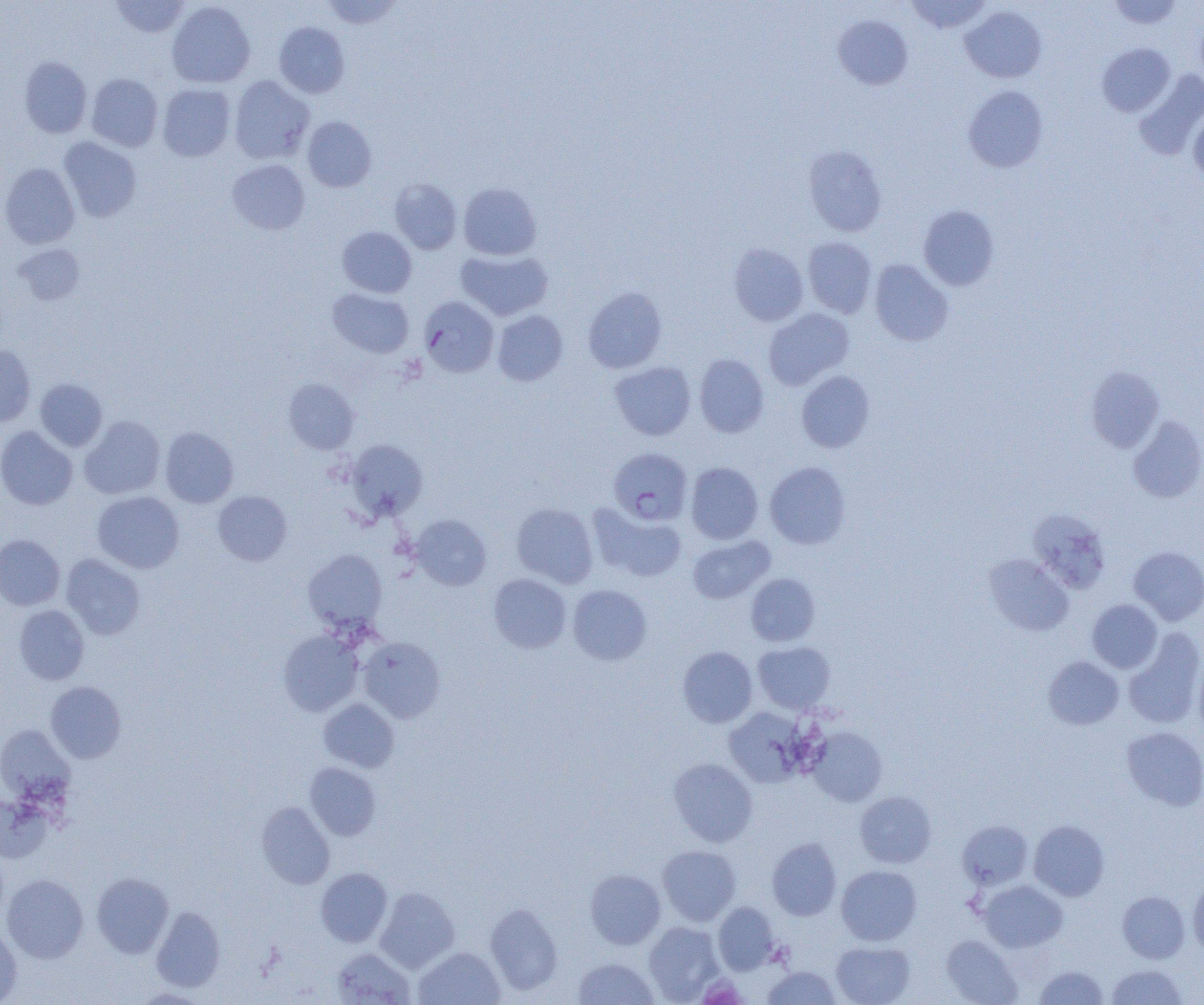

slide-level diagnosis = Plasmodium falciparum
image size = 1204×1005 pixels
modality = light microscopy
magnification = 1000x
field of view = one of a larger specimen
Plasmodium falciparum-infected red blood cell locations = approximate bounding boxes as [x1, y1, x2, y2] in pixels: [419, 296, 499, 377], [608, 447, 692, 525]
preparation = thin blood smear
uninfected red blood cell locations = approximate bounding boxes as [x1, y1, x2, y2] in pixels: [110, 0, 191, 38], [321, 0, 404, 29], [905, 0, 992, 34], [1107, 0, 1183, 29], [167, 1, 255, 88], [960, 5, 1046, 83], [834, 15, 913, 90], [274, 22, 350, 98], [1097, 43, 1175, 117], [19, 56, 92, 138], [1133, 71, 1204, 159], [86, 73, 163, 152], [229, 76, 314, 164], [157, 84, 236, 162], [963, 85, 1048, 172], [1188, 109, 1204, 185], [302, 116, 377, 192], [58, 137, 142, 222], [803, 146, 887, 236], [227, 159, 310, 235], [0, 163, 80, 249], [389, 178, 462, 254], [458, 182, 542, 260], [918, 205, 999, 290], [337, 226, 416, 297], [803, 237, 877, 318], [729, 243, 808, 326], [13, 244, 85, 306], [455, 249, 553, 320], [869, 259, 953, 346], [583, 286, 667, 373], [328, 288, 413, 358], [763, 308, 854, 390], [492, 310, 568, 386], [0, 345, 36, 426], [694, 353, 769, 437], [610, 361, 695, 441], [1086, 365, 1164, 453], [796, 370, 875, 452], [35, 378, 108, 451], [284, 378, 359, 454], [79, 415, 165, 499], [1128, 416, 1204, 503], [0, 426, 77, 510], [160, 427, 239, 508], [345, 439, 428, 521], [764, 461, 851, 549], [686, 462, 763, 544], [92, 490, 184, 573], [213, 490, 292, 566], [511, 503, 598, 588], [589, 505, 687, 583], [1028, 507, 1111, 594], [410, 514, 491, 590], [0, 534, 64, 610], [687, 535, 774, 604], [1128, 546, 1204, 625], [303, 549, 387, 633], [61, 554, 145, 640], [984, 554, 1074, 636], [488, 573, 571, 653], [746, 573, 820, 646], [568, 584, 653, 665], [1087, 599, 1162, 673], [14, 605, 89, 684], [1124, 629, 1204, 728], [278, 630, 364, 716], [358, 636, 445, 723], [753, 641, 836, 714], [677, 646, 757, 728], [1193, 652, 1204, 739], [1042, 656, 1124, 730], [46, 681, 126, 763], [319, 698, 399, 773], [724, 707, 808, 787], [0, 725, 75, 805], [806, 726, 887, 806], [1121, 726, 1204, 811], [668, 758, 758, 846], [305, 762, 381, 840], [855, 791, 936, 868], [0, 794, 52, 863], [256, 801, 335, 889], [957, 820, 1033, 890], [1029, 820, 1110, 901], [767, 837, 842, 921], [657, 845, 741, 926], [836, 865, 921, 945], [316, 867, 392, 947], [585, 868, 666, 949], [92, 872, 173, 958], [2, 874, 89, 963], [1188, 879, 1204, 957], [978, 880, 1068, 952], [376, 887, 459, 972], [1117, 891, 1190, 963], [485, 902, 563, 995], [713, 902, 780, 974], [151, 906, 225, 991], [643, 921, 723, 1002], [0, 925, 22, 1004], [941, 934, 1022, 1004], [831, 941, 916, 1005], [331, 947, 414, 1004], [414, 947, 504, 1005], [572, 957, 659, 1005], [1106, 964, 1188, 1005], [762, 965, 840, 1005], [1033, 965, 1109, 1005], [131, 987, 212, 1004]